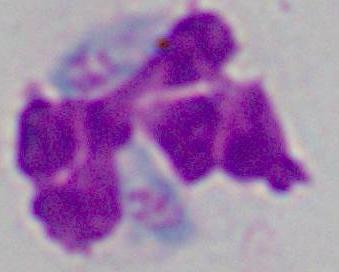

modality = photomicrograph
identification = leukocyte
magnification = 1000x